Locate and identify every blood parasite.
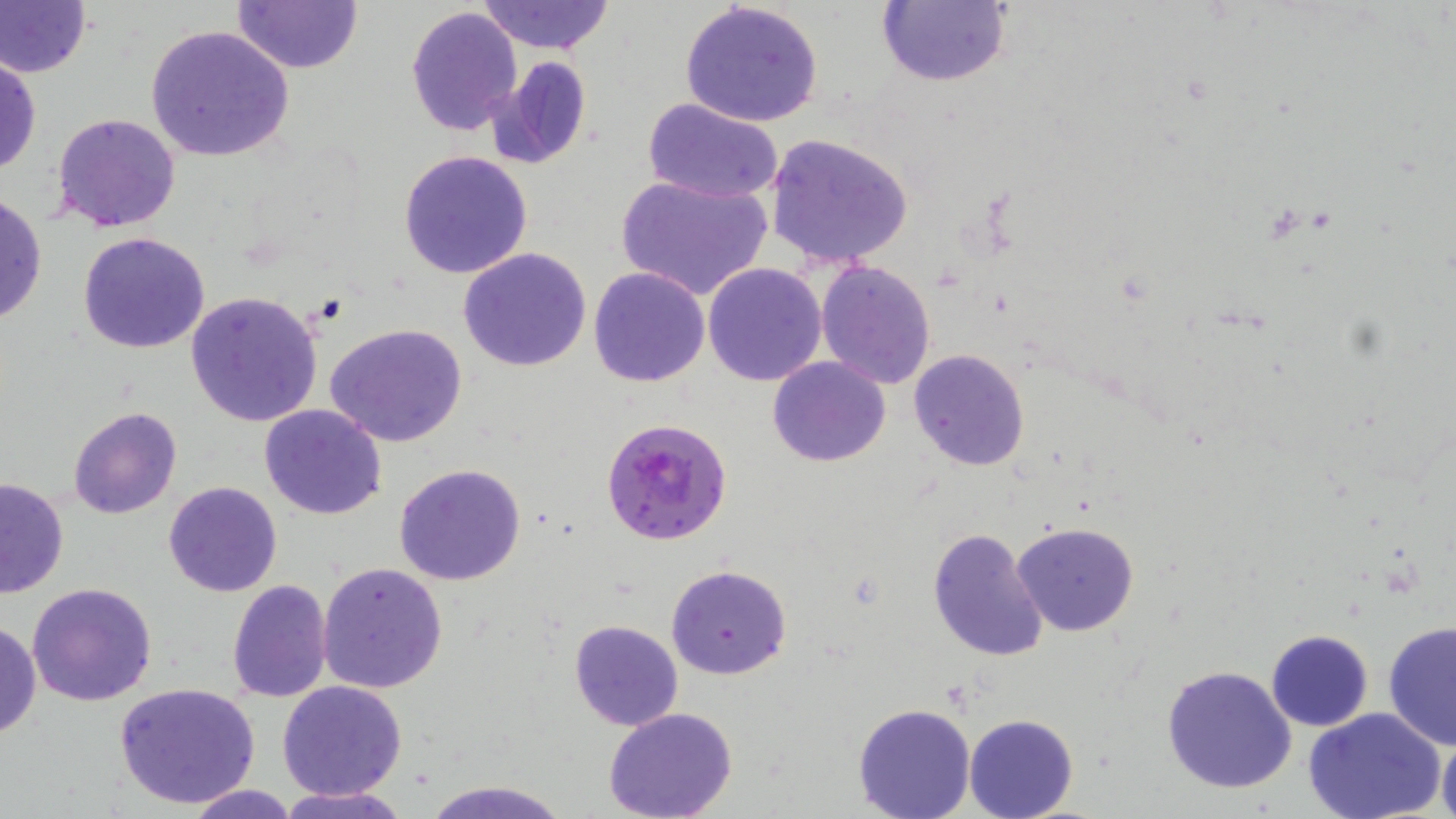
Approximate bounding boxes as [x1, y1, x2, y2] in pixels.
Plasmodium falciparum-infected red blood cells: [601, 416, 733, 544].
No Plasmodium ovale, Plasmodium malariae, Plasmodium vivax, Babesia divergens, or Trypanosoma brucei observed.

Summary:
  - Uninfected red blood cell locations: [0, 0, 91, 79], [877, 0, 1009, 88], [233, 1, 364, 73], [474, 1, 615, 53], [680, 2, 825, 129], [406, 5, 522, 134], [144, 24, 295, 162], [1, 52, 41, 178], [496, 55, 593, 167], [643, 98, 785, 202], [51, 113, 182, 231], [764, 131, 915, 270], [398, 151, 534, 279], [616, 172, 773, 300], [0, 192, 47, 328], [78, 232, 211, 354], [457, 246, 592, 371], [817, 259, 937, 389], [703, 262, 828, 386], [589, 266, 710, 387], [185, 291, 325, 429], [325, 323, 469, 448], [908, 348, 1030, 471], [769, 357, 891, 468], [258, 403, 387, 520], [68, 406, 182, 520], [393, 463, 526, 587], [0, 478, 70, 598], [163, 481, 282, 598], [1013, 523, 1140, 637], [928, 527, 1050, 664], [317, 562, 448, 693], [665, 565, 793, 680], [27, 580, 158, 706], [227, 580, 333, 702], [569, 619, 684, 732], [0, 620, 41, 740], [1382, 622, 1456, 749], [1265, 630, 1373, 731], [1161, 664, 1298, 794], [277, 680, 407, 801], [114, 683, 262, 808], [852, 703, 976, 819], [1304, 708, 1446, 819], [604, 710, 738, 819], [964, 715, 1078, 819], [1437, 731, 1456, 819], [421, 779, 568, 819], [181, 784, 303, 818], [275, 786, 412, 819]
  - Slide-level diagnosis: Plasmodium falciparum
  - Modality: optical microscopy
  - Magnification: 1000x
  - Field of view: single
  - Image size: 1456×819 pixels
  - Preparation: thin blood smear
  - Stain: May-Grünwald-Giemsa